Assess this cell for malaria.
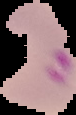

It is parasitized.

image size = 76×115 pixels
preparation = thin blood film
image type = segmented cell region with the area outside set to black